Report the malaria status of this cell.
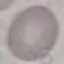
It is uninfected.

preparation = thin blood film
capture = smartphone camera at the microscope eyepiece
stain = Giemsa
image type = automatically extracted cell patch, resized to 64 × 64 pixels